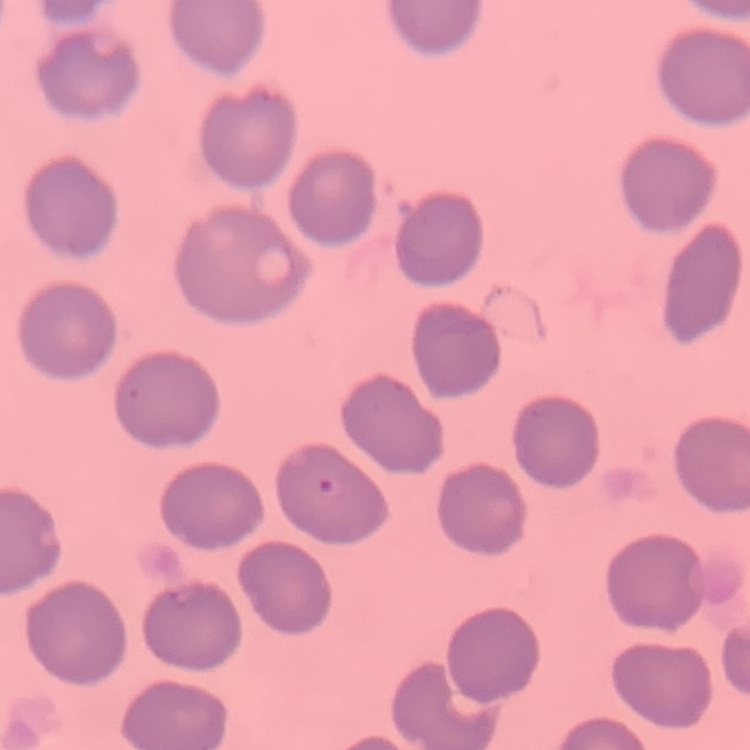

erythrocyte morphology = no rouleaux formation
preparation = thin peripheral smear
stain = Field's or Giemsa
image type = square crop of a larger photomicrograph